Identify the cell.
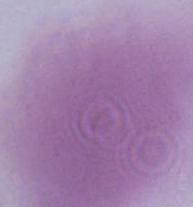

This is an erythrocyte.

1000x magnification. Photomicrograph.